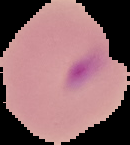

image type = segmented cell region on a black background
image size = 130×145 pixels
preparation = thin blood film
malaria status = parasitized